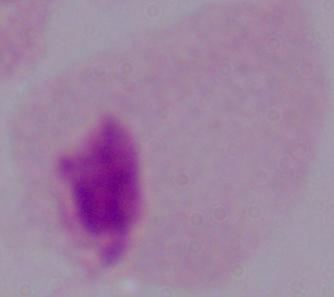
magnification = 1000x
identification = trichomonad
modality = micrograph